Assess the morphology of the erythrocytes.
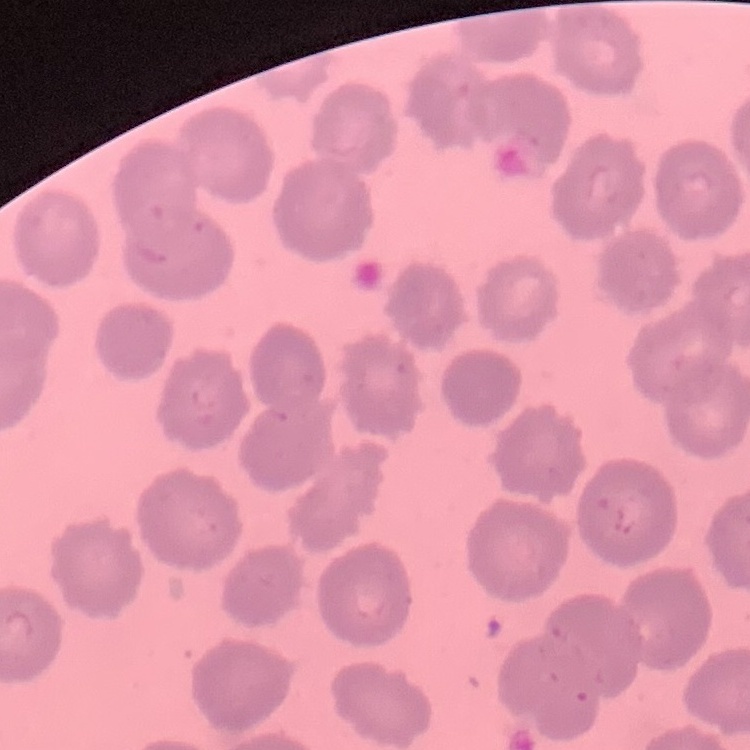

No rouleaux formation.

Thin blood film. One tile cut from a larger photomicrograph. Stained with either Field's or Giemsa.